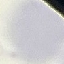
Summary:
  - Malaria status: uninfected
  - Stain: Giemsa
  - Capture: smartphone camera at the microscope eyepiece
  - Image type: cell patch, automatically extracted from a larger field of view and resized to 64 × 64 pixels
  - Preparation: thin blood smear